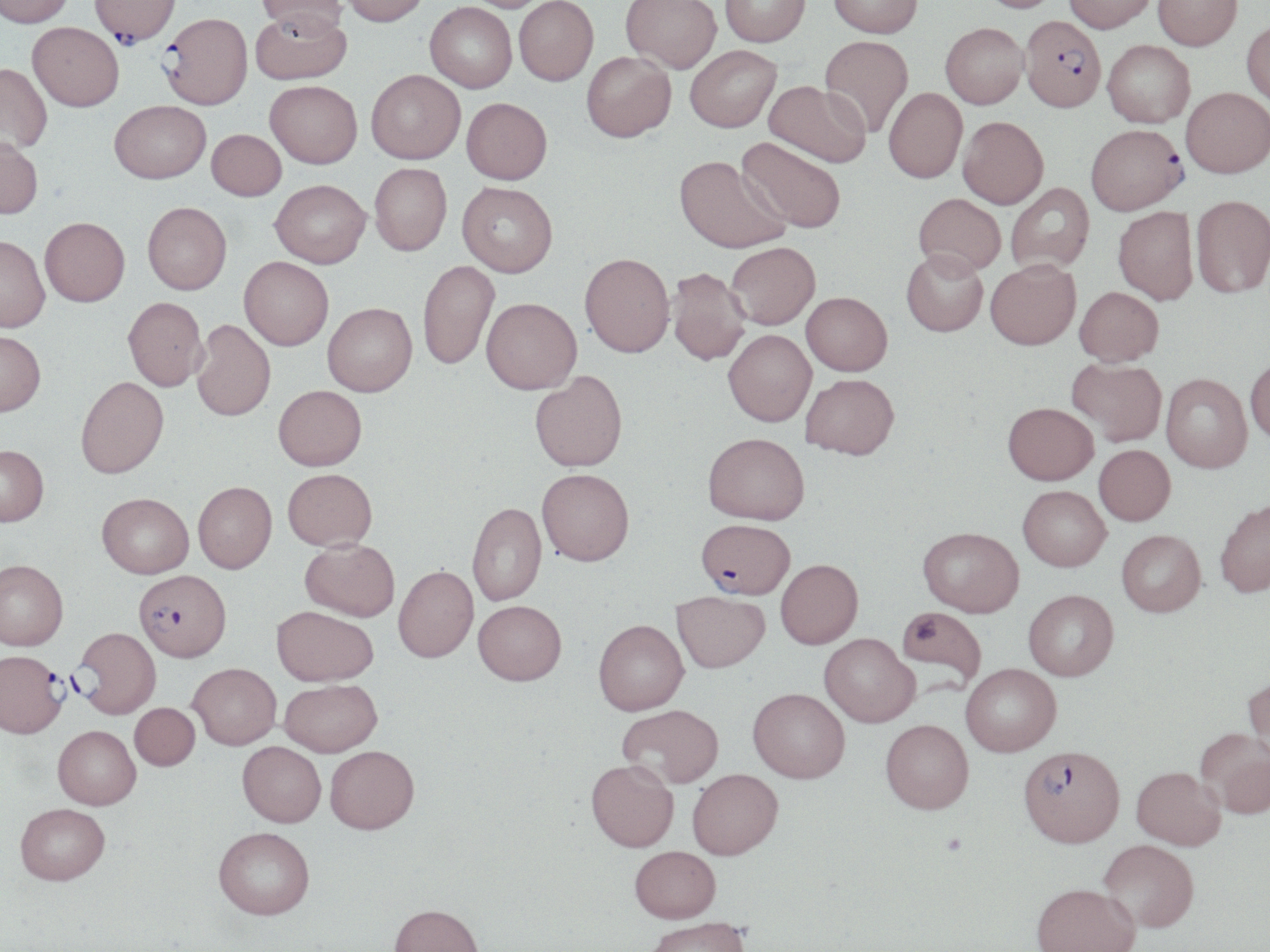
slide-level diagnosis = Plasmodium falciparum
platelet locations = approximate bounding boxes as named x1/y1/x2/y2 corners in pixels: (x1=941, y1=834, x2=966, y2=856)
field of view = one of a larger specimen
preparation = thin blood smear
magnification = 1000x
Plasmodium falciparum-infected red blood cell locations = approximate bounding boxes as named x1/y1/x2/y2 corners in pixels: (x1=91, y1=0, x2=179, y2=49), (x1=255, y1=0, x2=346, y2=39), (x1=161, y1=16, x2=254, y2=112), (x1=1020, y1=21, x2=1106, y2=116), (x1=1086, y1=127, x2=1187, y2=219), (x1=697, y1=520, x2=793, y2=601), (x1=134, y1=569, x2=231, y2=661), (x1=72, y1=627, x2=161, y2=718), (x1=0, y1=649, x2=68, y2=738), (x1=1019, y1=748, x2=1124, y2=851)
modality = optical microscopy
stain = May-Grünwald-Giemsa
uninfected red blood cell locations = approximate bounding boxes as named x1/y1/x2/y2 corners in pixels: (x1=0, y1=0, x2=74, y2=30), (x1=340, y1=0, x2=429, y2=30), (x1=460, y1=0, x2=554, y2=13), (x1=514, y1=0, x2=598, y2=87), (x1=621, y1=0, x2=722, y2=75), (x1=720, y1=0, x2=810, y2=48), (x1=828, y1=0, x2=923, y2=40), (x1=976, y1=0, x2=1064, y2=16), (x1=1064, y1=0, x2=1157, y2=36), (x1=1153, y1=0, x2=1242, y2=52), (x1=425, y1=3, x2=517, y2=95), (x1=251, y1=11, x2=352, y2=86), (x1=1242, y1=21, x2=1270, y2=108), (x1=27, y1=25, x2=123, y2=115), (x1=941, y1=26, x2=1028, y2=111), (x1=820, y1=37, x2=914, y2=138), (x1=1102, y1=41, x2=1194, y2=131), (x1=686, y1=47, x2=781, y2=135), (x1=582, y1=54, x2=676, y2=145), (x1=0, y1=66, x2=51, y2=156), (x1=366, y1=71, x2=465, y2=166), (x1=764, y1=81, x2=871, y2=170), (x1=265, y1=83, x2=362, y2=171), (x1=884, y1=89, x2=967, y2=184), (x1=1181, y1=89, x2=1270, y2=181), (x1=462, y1=99, x2=552, y2=187), (x1=109, y1=102, x2=211, y2=187), (x1=958, y1=118, x2=1049, y2=210), (x1=207, y1=130, x2=286, y2=202), (x1=736, y1=137, x2=846, y2=235), (x1=0, y1=139, x2=43, y2=221), (x1=674, y1=158, x2=790, y2=256), (x1=369, y1=164, x2=452, y2=258), (x1=271, y1=181, x2=371, y2=270), (x1=457, y1=184, x2=557, y2=279), (x1=1006, y1=184, x2=1095, y2=275), (x1=913, y1=194, x2=1004, y2=279), (x1=1191, y1=197, x2=1270, y2=300), (x1=143, y1=204, x2=232, y2=296), (x1=1113, y1=208, x2=1198, y2=306), (x1=40, y1=220, x2=130, y2=310), (x1=0, y1=239, x2=49, y2=335), (x1=726, y1=242, x2=820, y2=330), (x1=901, y1=250, x2=988, y2=337), (x1=579, y1=255, x2=674, y2=360), (x1=239, y1=258, x2=333, y2=352), (x1=418, y1=260, x2=499, y2=371), (x1=985, y1=260, x2=1081, y2=352), (x1=667, y1=269, x2=751, y2=367), (x1=1074, y1=287, x2=1163, y2=367), (x1=801, y1=292, x2=892, y2=376), (x1=123, y1=298, x2=208, y2=392), (x1=481, y1=298, x2=581, y2=395), (x1=322, y1=303, x2=417, y2=397), (x1=190, y1=320, x2=275, y2=422), (x1=723, y1=329, x2=816, y2=427), (x1=0, y1=331, x2=45, y2=417), (x1=1067, y1=358, x2=1166, y2=445), (x1=1246, y1=358, x2=1270, y2=445), (x1=530, y1=372, x2=627, y2=472), (x1=801, y1=373, x2=899, y2=459), (x1=1161, y1=374, x2=1252, y2=473), (x1=75, y1=376, x2=169, y2=479), (x1=273, y1=385, x2=367, y2=470), (x1=1003, y1=402, x2=1099, y2=485), (x1=703, y1=432, x2=809, y2=524), (x1=1094, y1=444, x2=1176, y2=526), (x1=0, y1=445, x2=49, y2=527), (x1=283, y1=468, x2=377, y2=551), (x1=537, y1=470, x2=634, y2=567), (x1=193, y1=482, x2=277, y2=573), (x1=1018, y1=487, x2=1110, y2=572), (x1=97, y1=493, x2=194, y2=579), (x1=1215, y1=498, x2=1270, y2=598), (x1=466, y1=502, x2=546, y2=606), (x1=917, y1=527, x2=1024, y2=619), (x1=1116, y1=530, x2=1206, y2=617), (x1=300, y1=540, x2=399, y2=622), (x1=775, y1=559, x2=863, y2=650), (x1=0, y1=560, x2=68, y2=650), (x1=393, y1=566, x2=478, y2=664), (x1=1024, y1=591, x2=1118, y2=683), (x1=672, y1=592, x2=769, y2=673), (x1=473, y1=602, x2=566, y2=688), (x1=271, y1=606, x2=378, y2=687), (x1=896, y1=607, x2=986, y2=691), (x1=593, y1=620, x2=689, y2=716), (x1=819, y1=635, x2=919, y2=728), (x1=188, y1=663, x2=281, y2=749), (x1=961, y1=665, x2=1061, y2=758), (x1=1243, y1=677, x2=1270, y2=765), (x1=279, y1=679, x2=382, y2=758), (x1=748, y1=688, x2=850, y2=784), (x1=130, y1=703, x2=199, y2=770), (x1=617, y1=704, x2=723, y2=789), (x1=881, y1=721, x2=973, y2=817), (x1=53, y1=725, x2=141, y2=809), (x1=1195, y1=728, x2=1270, y2=819), (x1=237, y1=741, x2=326, y2=828), (x1=325, y1=745, x2=419, y2=834), (x1=586, y1=761, x2=678, y2=853), (x1=1131, y1=767, x2=1226, y2=850), (x1=688, y1=769, x2=783, y2=861), (x1=15, y1=802, x2=110, y2=884), (x1=213, y1=827, x2=315, y2=920), (x1=1098, y1=839, x2=1199, y2=934), (x1=629, y1=846, x2=720, y2=925), (x1=1030, y1=885, x2=1140, y2=952), (x1=388, y1=904, x2=484, y2=952), (x1=641, y1=917, x2=751, y2=951)
image size = 1270×952 pixels